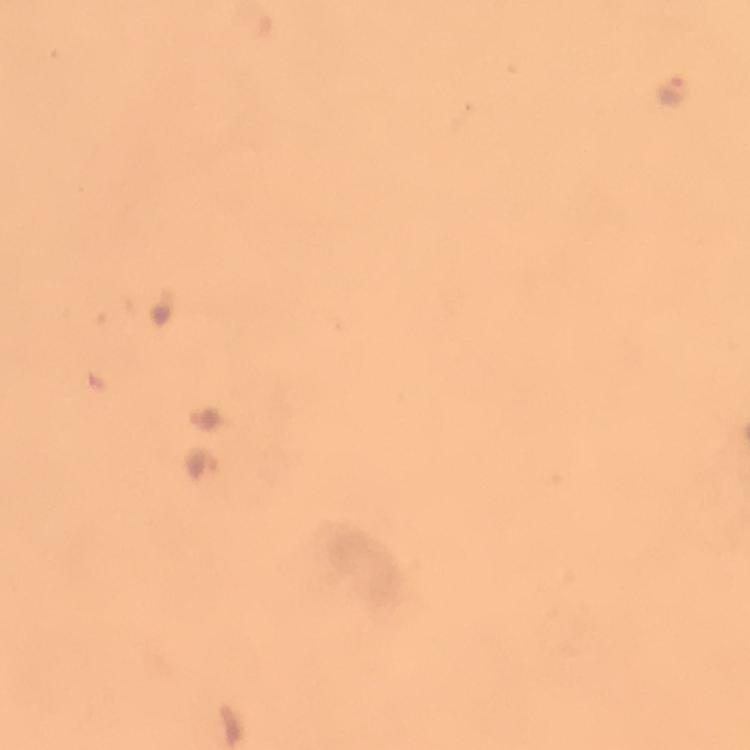

immersion oil = applied
Plasmodium parasite locations = approximate centers as (x, y) in pixels: (671, 85), (207, 417), (207, 466)
cropped from = one field of view
context = from a malaria diagnostic workup
capture = smartphone camera through the microscope
preparation = thick smear
image size = 750×750 pixels
magnification = 100x
stain = Giemsa